Locate every blood parasite and identify its species.
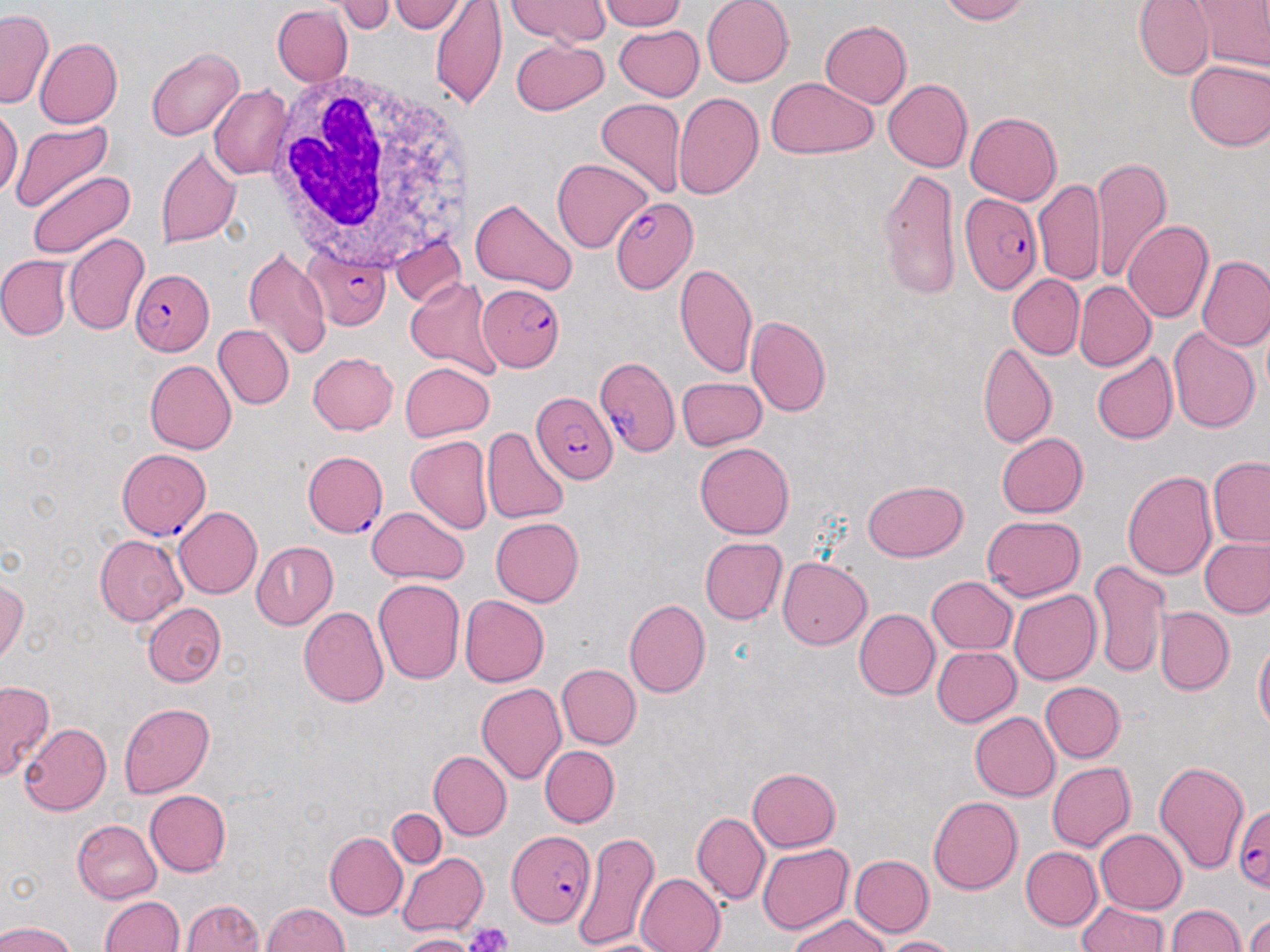
Approximate bounding boxes as named x1/y1/x2/y2 corners in pixels.
Plasmodium falciparum-infected red blood cells: (x1=960, y1=193, x2=1043, y2=295), (x1=611, y1=196, x2=699, y2=294), (x1=306, y1=247, x2=391, y2=331), (x1=130, y1=271, x2=214, y2=353), (x1=476, y1=284, x2=564, y2=372), (x1=594, y1=354, x2=682, y2=459), (x1=531, y1=392, x2=618, y2=485), (x1=115, y1=447, x2=211, y2=540), (x1=302, y1=450, x2=389, y2=538), (x1=1227, y1=798, x2=1270, y2=890), (x1=504, y1=829, x2=596, y2=927).
No Plasmodium ovale, Plasmodium malariae, Plasmodium vivax, Babesia divergens, or Trypanosoma brucei observed.

Platelet locations: (x1=465, y1=922, x2=513, y2=952). Uninfected red blood cell locations: (x1=340, y1=0, x2=396, y2=32), (x1=390, y1=0, x2=465, y2=35), (x1=598, y1=0, x2=691, y2=31), (x1=702, y1=0, x2=793, y2=86), (x1=935, y1=0, x2=1030, y2=24), (x1=1135, y1=0, x2=1212, y2=78), (x1=1192, y1=0, x2=1268, y2=72), (x1=430, y1=1, x2=506, y2=108), (x1=509, y1=2, x2=612, y2=46), (x1=270, y1=4, x2=351, y2=84), (x1=0, y1=10, x2=53, y2=108), (x1=818, y1=19, x2=910, y2=108), (x1=613, y1=22, x2=704, y2=101), (x1=34, y1=37, x2=123, y2=127), (x1=510, y1=41, x2=610, y2=115), (x1=144, y1=47, x2=243, y2=142), (x1=1184, y1=59, x2=1270, y2=152), (x1=765, y1=77, x2=875, y2=159), (x1=882, y1=78, x2=971, y2=173), (x1=209, y1=83, x2=292, y2=179), (x1=673, y1=90, x2=765, y2=199), (x1=595, y1=99, x2=686, y2=201), (x1=0, y1=108, x2=20, y2=205), (x1=964, y1=111, x2=1064, y2=205), (x1=11, y1=118, x2=115, y2=213), (x1=155, y1=144, x2=242, y2=251), (x1=1091, y1=156, x2=1171, y2=282), (x1=551, y1=158, x2=652, y2=251), (x1=877, y1=169, x2=963, y2=298), (x1=25, y1=171, x2=135, y2=259), (x1=1035, y1=177, x2=1105, y2=288), (x1=471, y1=197, x2=576, y2=296), (x1=1121, y1=220, x2=1212, y2=324), (x1=62, y1=231, x2=149, y2=336), (x1=243, y1=247, x2=330, y2=360), (x1=1197, y1=253, x2=1270, y2=352), (x1=1, y1=255, x2=72, y2=338), (x1=674, y1=263, x2=758, y2=381), (x1=1007, y1=274, x2=1084, y2=360), (x1=407, y1=275, x2=500, y2=377), (x1=1074, y1=281, x2=1156, y2=372), (x1=746, y1=314, x2=831, y2=415), (x1=216, y1=324, x2=292, y2=408), (x1=1168, y1=326, x2=1259, y2=434), (x1=980, y1=341, x2=1059, y2=449), (x1=305, y1=349, x2=400, y2=436), (x1=1091, y1=352, x2=1177, y2=445), (x1=145, y1=360, x2=239, y2=453), (x1=399, y1=361, x2=494, y2=441), (x1=676, y1=376, x2=766, y2=451), (x1=481, y1=429, x2=567, y2=526), (x1=994, y1=431, x2=1086, y2=518), (x1=406, y1=434, x2=493, y2=537), (x1=694, y1=444, x2=793, y2=538), (x1=1209, y1=457, x2=1270, y2=547), (x1=1122, y1=469, x2=1218, y2=580), (x1=861, y1=480, x2=966, y2=562), (x1=172, y1=506, x2=262, y2=600), (x1=367, y1=506, x2=468, y2=586), (x1=981, y1=515, x2=1087, y2=602), (x1=489, y1=517, x2=583, y2=606), (x1=92, y1=532, x2=187, y2=626), (x1=1201, y1=535, x2=1270, y2=616), (x1=698, y1=537, x2=786, y2=625), (x1=249, y1=542, x2=338, y2=627), (x1=777, y1=557, x2=871, y2=649), (x1=1087, y1=557, x2=1170, y2=677), (x1=0, y1=570, x2=28, y2=667), (x1=927, y1=576, x2=1019, y2=656), (x1=373, y1=578, x2=466, y2=687), (x1=1008, y1=589, x2=1102, y2=684), (x1=459, y1=594, x2=549, y2=687), (x1=626, y1=597, x2=709, y2=696), (x1=141, y1=601, x2=226, y2=685), (x1=298, y1=605, x2=388, y2=708), (x1=853, y1=608, x2=938, y2=700), (x1=1157, y1=608, x2=1233, y2=695), (x1=1253, y1=637, x2=1268, y2=738), (x1=931, y1=643, x2=1023, y2=726), (x1=556, y1=663, x2=640, y2=750), (x1=1, y1=681, x2=56, y2=782), (x1=1041, y1=681, x2=1128, y2=762), (x1=476, y1=683, x2=567, y2=786), (x1=118, y1=700, x2=214, y2=797), (x1=969, y1=711, x2=1062, y2=801), (x1=18, y1=722, x2=112, y2=814), (x1=539, y1=745, x2=619, y2=827), (x1=427, y1=750, x2=510, y2=839), (x1=1152, y1=760, x2=1250, y2=878), (x1=1045, y1=762, x2=1134, y2=852), (x1=748, y1=767, x2=841, y2=851), (x1=143, y1=788, x2=231, y2=876), (x1=928, y1=793, x2=1023, y2=894), (x1=385, y1=809, x2=446, y2=869), (x1=691, y1=811, x2=769, y2=907), (x1=72, y1=819, x2=164, y2=902), (x1=1096, y1=829, x2=1186, y2=910), (x1=573, y1=830, x2=658, y2=951), (x1=324, y1=833, x2=406, y2=917), (x1=756, y1=841, x2=855, y2=935), (x1=1021, y1=847, x2=1101, y2=930), (x1=396, y1=850, x2=489, y2=936), (x1=853, y1=854, x2=932, y2=936), (x1=635, y1=874, x2=724, y2=952), (x1=100, y1=895, x2=184, y2=952), (x1=183, y1=896, x2=266, y2=952), (x1=1075, y1=899, x2=1169, y2=952), (x1=260, y1=902, x2=352, y2=952), (x1=1169, y1=902, x2=1244, y2=952), (x1=786, y1=914, x2=889, y2=952), (x1=1242, y1=918, x2=1270, y2=952), (x1=0, y1=922, x2=79, y2=952), (x1=394, y1=932, x2=483, y2=951), (x1=880, y1=935, x2=958, y2=951). White blood cell locations: (x1=266, y1=64, x2=484, y2=282). Slide-level diagnosis: Plasmodium falciparum. One field of a larger specimen. Light microscopy. Thin blood smear. 1000x magnification. Image is 1270×952 pixels. May-Grünwald-Giemsa stain.